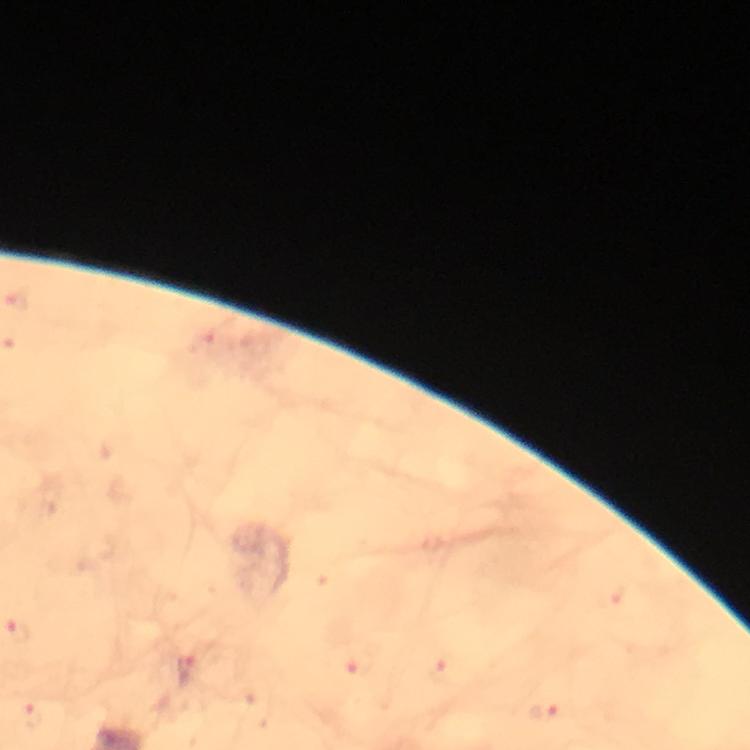
stain: Giemsa
capture: smartphone camera through the microscope
image_size: 750×750 pixels
context: from a diagnostic examination for malaria
magnification: 100x
immersion_oil: used
malaria_parasite_locations: 'approximate object centers, in pixels from the top-left corner: (x=18, y=631), (x=188, y=673), (x=545, y=712)'
preparation: thick blood smear
cropped_from: one field of view